State which parasite is depicted.
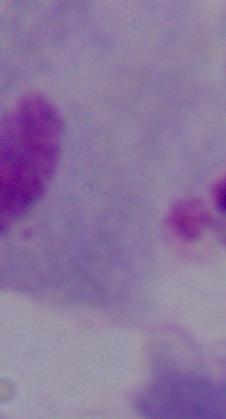

This is a trichomonad.

Captured at 1000x magnification. Photomicrograph.